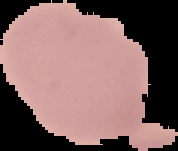
image type = cell region segmented out of the field of view; surrounding area masked to black
image size = 178×151 pixels
preparation = thin blood film
result = no malaria parasites seen